Locate every parasitized red blood cell.
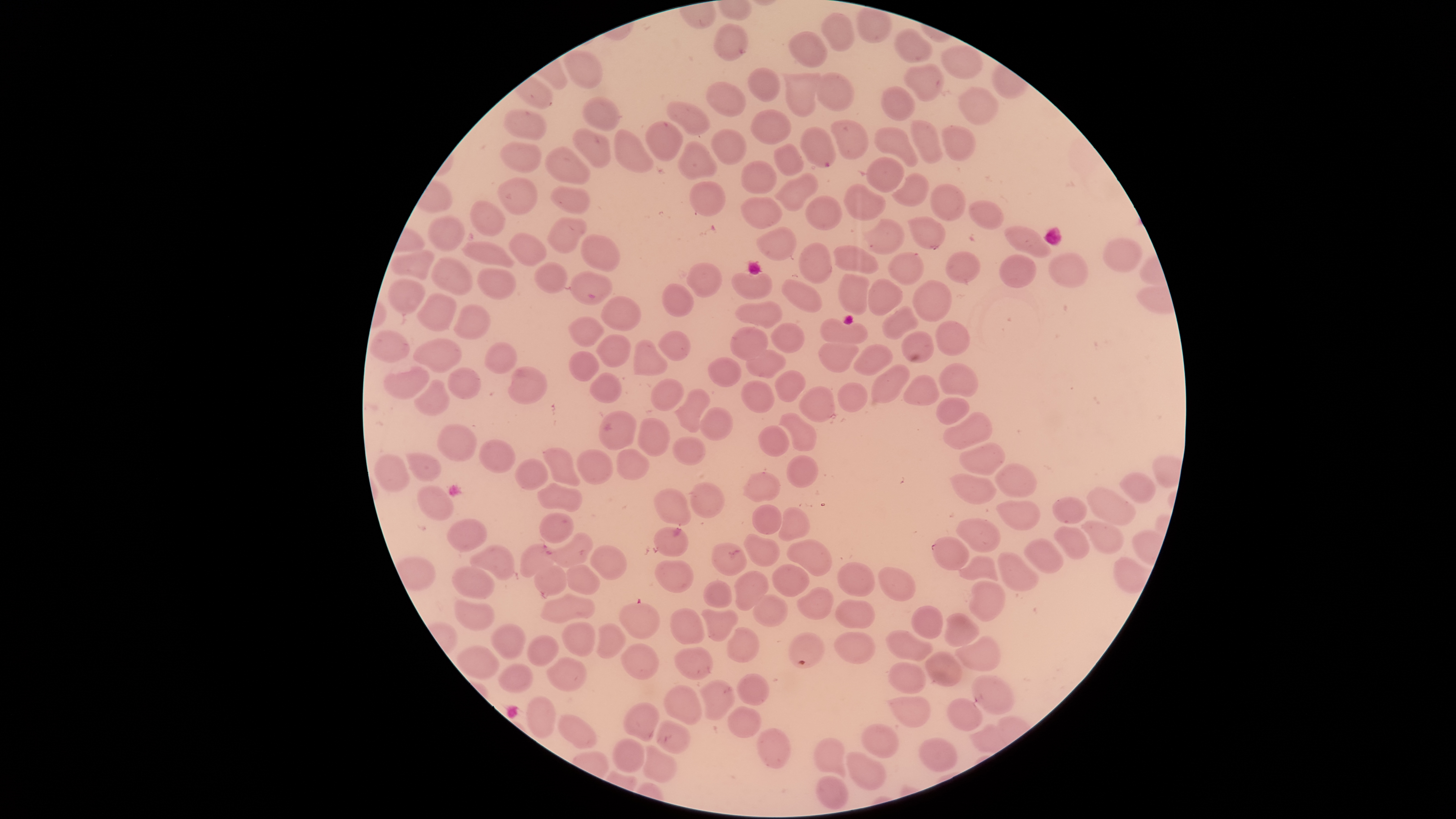

Approximate bounding boxes as {left, top, right, bottom} in pixels.
Parasitized red blood cells: {800, 129, 834, 166}, {550, 532, 595, 567}, {932, 536, 970, 570}, {519, 544, 557, 577}, {619, 602, 660, 639}.

{
  "preparation": "thin blood smear",
  "species": "Plasmodium falciparum",
  "uninfected_red_blood_cells": "approximate bounding boxes as {left, top, right, bottom} in pixels: {822, 14, 854, 53}, {713, 23, 747, 60}, {895, 29, 931, 63}, {790, 32, 828, 68}, {941, 46, 983, 79}, {564, 50, 603, 89}, {904, 64, 943, 100}, {747, 67, 781, 102}, {783, 71, 820, 118}, {816, 73, 856, 110}, {706, 82, 746, 117}, {884, 86, 914, 121}, {960, 87, 996, 123}, {583, 96, 622, 130}, {667, 102, 710, 135}, {752, 109, 792, 145}, {502, 110, 548, 140}, {830, 120, 867, 158}, {911, 120, 942, 163}, {646, 121, 682, 161}, {940, 124, 975, 160}, {875, 128, 919, 167}, {573, 129, 611, 168}, {613, 130, 653, 172}, {711, 130, 747, 165}, {676, 141, 716, 180}, {502, 143, 540, 172}, {774, 144, 803, 175}, {546, 145, 591, 183}, {866, 157, 907, 191}, {740, 161, 777, 194}, {779, 174, 818, 211}, {892, 174, 928, 205}, {499, 178, 536, 215}, {689, 180, 726, 217}, {845, 183, 886, 221}, {929, 183, 965, 221}, {550, 185, 590, 214}, {805, 195, 842, 230}, {742, 197, 781, 228}, {470, 200, 505, 235}, {969, 200, 1004, 230}, {429, 215, 467, 252}, {548, 216, 586, 255}, {909, 217, 945, 248}, {865, 220, 907, 254}, {1005, 224, 1051, 259}, {757, 228, 795, 259}, {509, 230, 546, 265}, {581, 234, 620, 272}, {1103, 238, 1142, 270}, {462, 242, 515, 267}, {799, 242, 831, 281}, {835, 244, 880, 275}, {391, 249, 434, 279}, {947, 249, 982, 285}, {888, 252, 924, 287}, {1000, 253, 1036, 288}, {1049, 253, 1087, 288}, {432, 257, 470, 294}, {532, 260, 568, 294}, {686, 264, 722, 297}, {478, 268, 515, 301}, {570, 271, 613, 305}, {731, 271, 772, 300}, {837, 274, 872, 317}, {866, 276, 906, 317}, {386, 278, 427, 314}, {782, 279, 822, 314}, {913, 279, 954, 321}, {661, 281, 694, 318}, {415, 294, 456, 331}, {601, 296, 642, 330}, {734, 300, 782, 328}, {882, 303, 920, 339}, {454, 305, 491, 337}, {568, 317, 604, 346}, {819, 319, 871, 346}, {935, 321, 970, 356}, {770, 323, 803, 353}, {732, 327, 768, 360}, {370, 331, 409, 360}, {658, 331, 691, 361}, {902, 331, 934, 363}, {596, 334, 631, 368}, {415, 337, 461, 372}, {633, 337, 670, 378}, {818, 339, 860, 372}, {486, 344, 515, 374}, {852, 344, 896, 377}, {745, 346, 787, 379}, {569, 352, 600, 381}, {708, 356, 740, 387}, {940, 361, 979, 398}, {870, 363, 911, 402}, {508, 366, 548, 404}, {384, 368, 429, 398}, {448, 368, 480, 399}, {775, 370, 806, 403}, {902, 375, 940, 406}, {414, 379, 450, 416}, {651, 379, 682, 411}, {741, 381, 774, 413}, {837, 382, 867, 412}, {799, 386, 834, 422}, {674, 389, 710, 433}, {935, 397, 971, 425}, {699, 407, 735, 441}, {598, 411, 636, 449}, {942, 411, 993, 450}, {779, 413, 816, 451}, {637, 417, 671, 456}, {436, 424, 476, 461}, {758, 425, 789, 457}, {673, 437, 704, 464}, {480, 438, 516, 473}, {960, 441, 1006, 475}, {544, 448, 581, 487}, {579, 448, 612, 484}, {616, 449, 649, 480}, {406, 452, 441, 482}, {376, 455, 408, 491}, {787, 456, 819, 489}, {517, 459, 547, 490}, {995, 463, 1037, 498}, {744, 471, 781, 504}, {1120, 472, 1156, 503}, {950, 473, 996, 505}, {691, 481, 727, 519}, {538, 482, 582, 513}, {417, 485, 454, 520}, {1088, 488, 1136, 525}, {653, 489, 690, 527}, {1053, 497, 1089, 525}, {997, 499, 1041, 530}, {751, 504, 783, 535}, {777, 508, 809, 542}, {541, 512, 574, 544}, {447, 518, 488, 551}, {956, 518, 1001, 552}, {1081, 520, 1123, 554}, {652, 527, 688, 559}, {1054, 527, 1089, 559}, {743, 534, 781, 568}, {1025, 538, 1064, 573}, {786, 540, 834, 578}, {712, 542, 748, 575}, {471, 545, 515, 579}, {590, 545, 626, 580}, {997, 552, 1036, 591}, {960, 555, 998, 584}, {655, 560, 695, 593}, {838, 562, 875, 597}, {534, 563, 567, 596}, {566, 564, 601, 595}, {771, 565, 809, 597}, {877, 565, 916, 602}, {454, 566, 495, 599}, {733, 570, 769, 610}, {701, 579, 732, 608}, {969, 580, 1006, 622}, {797, 587, 832, 620}, {539, 594, 596, 621}, {752, 594, 788, 626}, {454, 600, 495, 629}, {835, 600, 874, 629}, {912, 605, 943, 639}, {699, 606, 739, 641}, {668, 608, 705, 644}, {943, 613, 980, 647}, {563, 623, 595, 657}, {593, 623, 625, 658}, {492, 624, 526, 660}, {726, 628, 758, 662}, {887, 629, 933, 662}, {834, 631, 875, 664}, {789, 632, 824, 668}, {528, 635, 559, 667}, {956, 635, 1001, 671}, {621, 644, 659, 679}, {458, 646, 498, 681}, {674, 648, 712, 679}, {926, 651, 962, 688}, {547, 656, 585, 690}, {890, 661, 926, 694}, {499, 662, 532, 692}, {735, 673, 770, 706}, {973, 674, 1015, 714}, {696, 679, 734, 721}, {662, 684, 704, 726}, {888, 695, 930, 728}, {526, 696, 556, 737}, {947, 698, 983, 732}, {624, 703, 658, 742}, {728, 705, 762, 739}, {559, 713, 596, 748}, {656, 720, 689, 753}, {862, 725, 898, 758}, {756, 728, 791, 769}, {613, 739, 643, 772}, {815, 739, 847, 778}, {920, 740, 955, 773}, {640, 745, 679, 781}, {846, 752, 885, 789}, {816, 776, 850, 809}",
  "visible_region": "circular",
  "stain": "Giemsa",
  "field_of_view": "single",
  "capture": "smartphone photograph through the microscope eyepiece",
  "image_size": "1456×819 pixels"
}